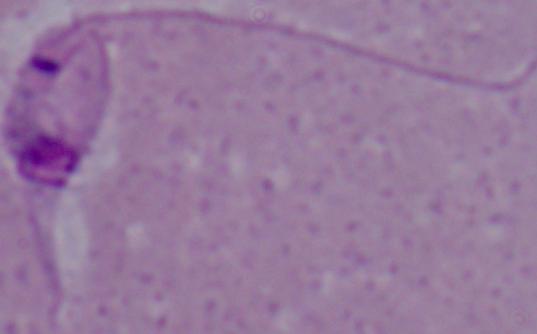

A Leishmania parasite is seen. Micrograph. 1000x magnification.